Describe the morphology of the red blood cells.
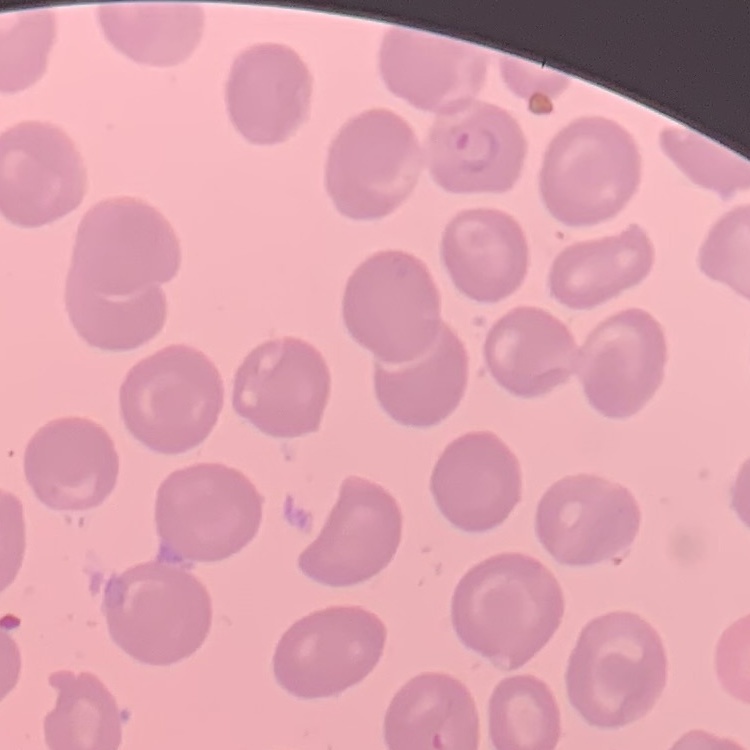
No rouleaux formation.

Thin blood film. Stained with either Field's or Giemsa. Square crop of a larger photomicrograph.